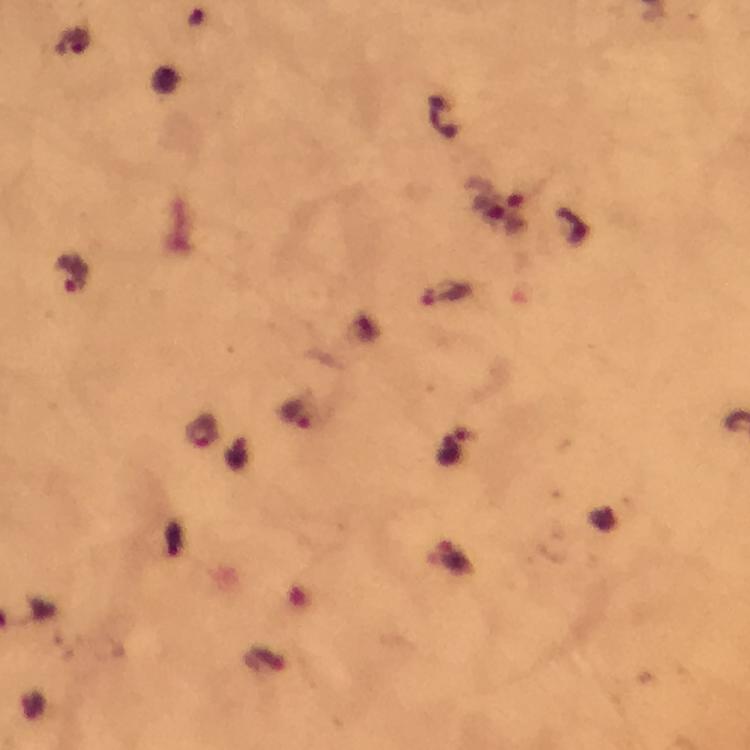
Approximate centers as (x, y) in pixels.
Summary:
  - Malaria parasite locations: (72, 273), (446, 294), (297, 414), (203, 433), (451, 557)
  - Preparation: thick smear
  - Magnification: 100x
  - Cropped from: one field of view
  - Capture: smartphone photograph through a microscope
  - Context: from a malaria diagnostic workup
  - Stain: Giemsa
  - Immersion oil: used
  - Image size: 750×750 pixels